Classify this cell by malaria status.
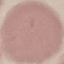
Uninfected.

Giemsa stain. Acquired by smartphone through the microscope eyepiece. Automatically extracted cell patch, resized to 64 × 64 pixels. Thin blood film.